Assess the morphology of the erythrocytes.
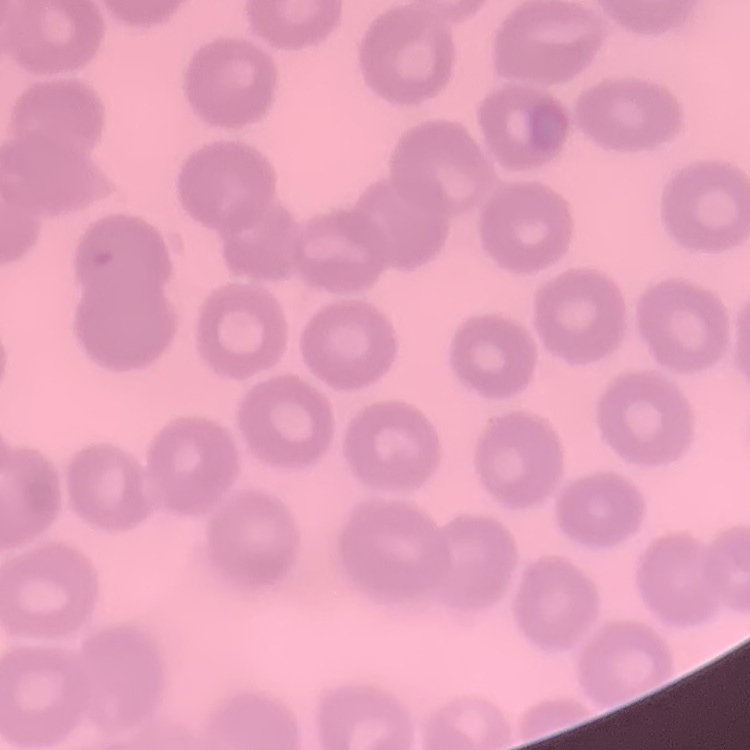
No rouleaux formation.

Summary:
  - Preparation: thin blood film
  - Image type: square crop of a larger photomicrograph
  - Stain: Field's or Giemsa